Report the malaria status of this cell.
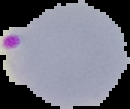

It is parasitized.

Image is 130×109 pixels. From a thin blood smear. The area outside the segmented cell region is set to black.